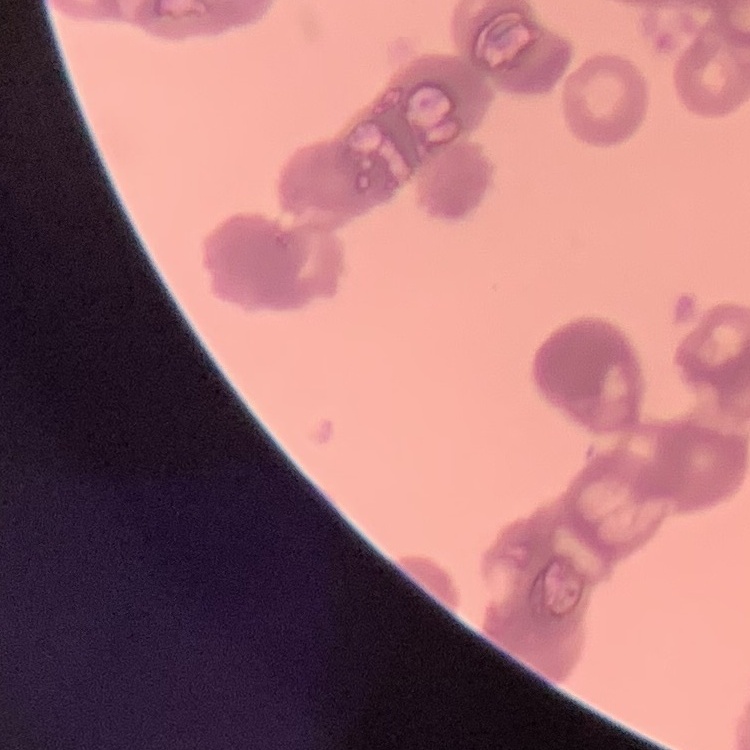
erythrocyte morphology = rouleaux formation
image type = square crop of a larger photomicrograph
preparation = thin peripheral smear
stain = Field's or Giemsa